Classify this cell by malaria status.
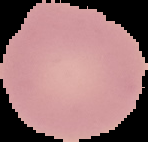

Uninfected.

From a thin blood smear. Image is 148×142 pixels. Cell region segmented out of the field of view; the surrounding area is masked to black.